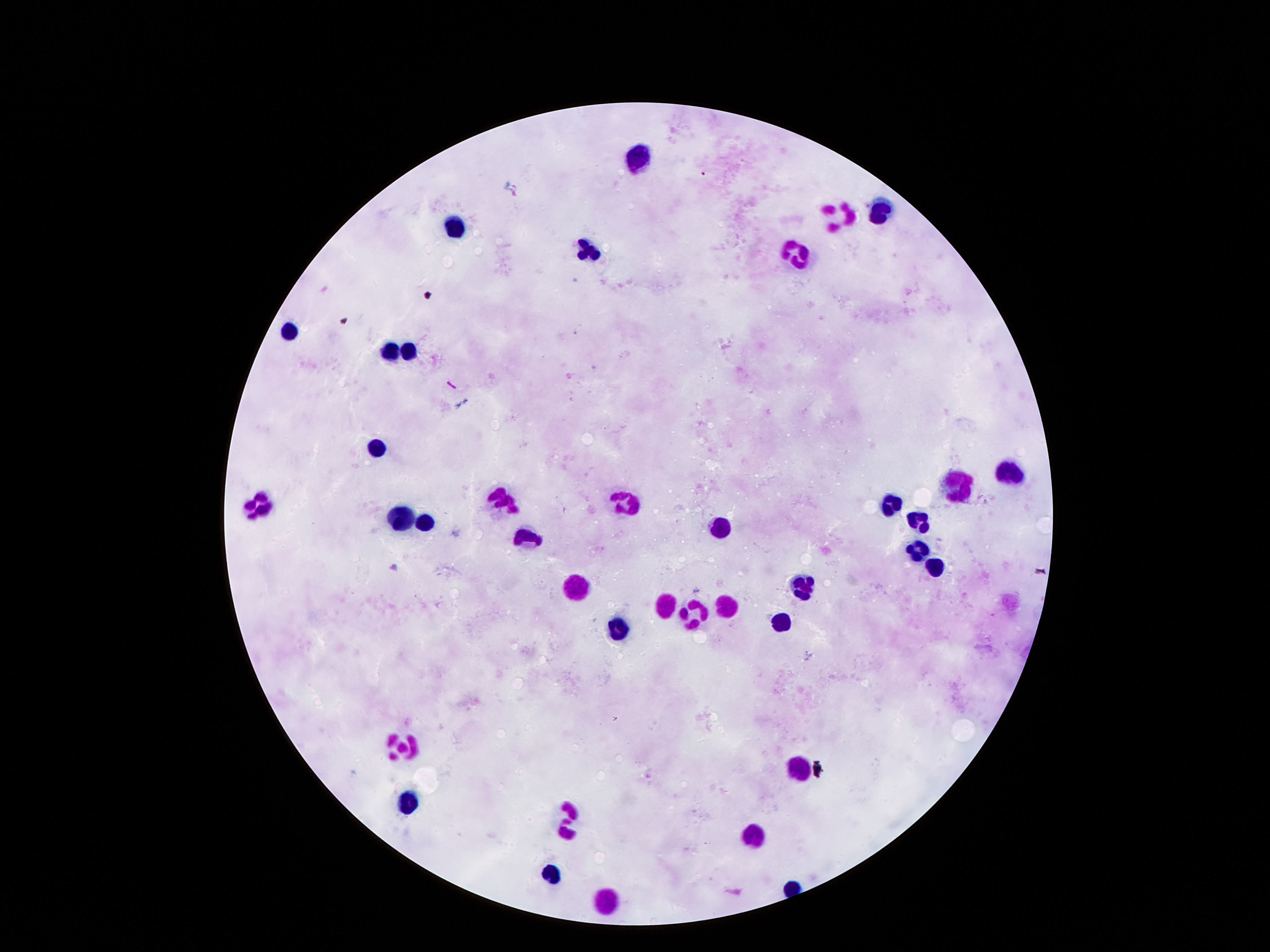
Approximate centers as (x, y) in pixels.
Summary:
  - Leukocyte locations: (644, 161), (882, 209), (834, 214), (449, 227), (585, 251), (788, 258), (287, 334), (407, 349), (390, 353), (380, 444), (1011, 471), (955, 484), (498, 496), (629, 502), (894, 504), (258, 505), (401, 519), (423, 522), (919, 525), (724, 532), (525, 537), (916, 545), (931, 568), (574, 583), (807, 589), (669, 600), (725, 605), (700, 612), (787, 621), (620, 630), (406, 741), (795, 767), (405, 803), (564, 821), (759, 838), (549, 870), (607, 899)
  - Patient malaria status: uninfected
  - Preparation: thick blood film
  - Stain: Giemsa
  - Field of view: single
  - Capture: smartphone camera through the microscope eyepiece
  - Image size: 1270×952 pixels
  - Magnification: 100x